Describe the morphology of the red blood cells.
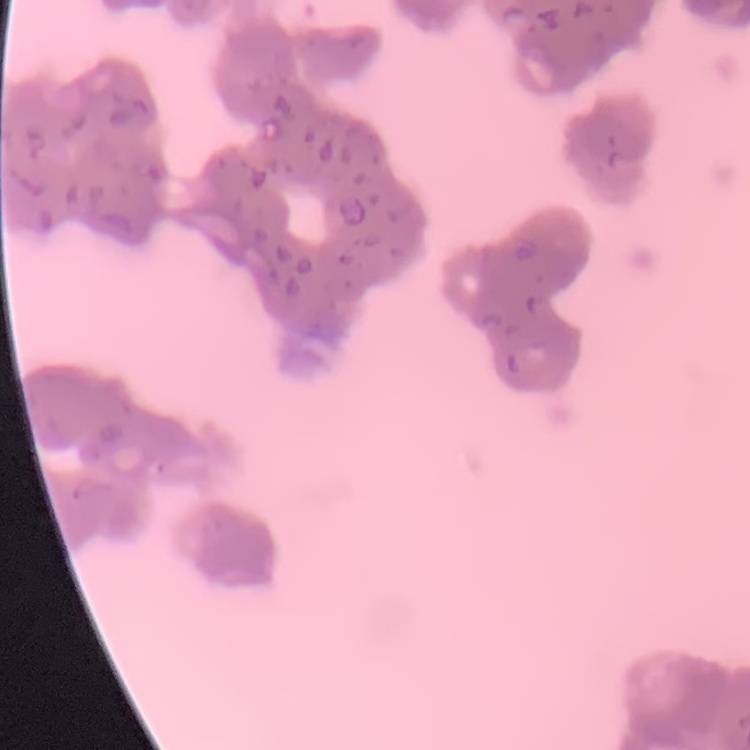
Rouleaux formation.

Summary:
  - Preparation: thin blood film
  - Stain: Field's or Giemsa
  - Image type: one tile cut from a larger photomicrograph